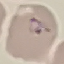 Result: malaria parasites identified. Photographed with a smartphone camera at the microscope eyepiece. Giemsa stain. Thin blood film. Cell patch, automatically extracted from a larger field of view and resized to 64 × 64 pixels.